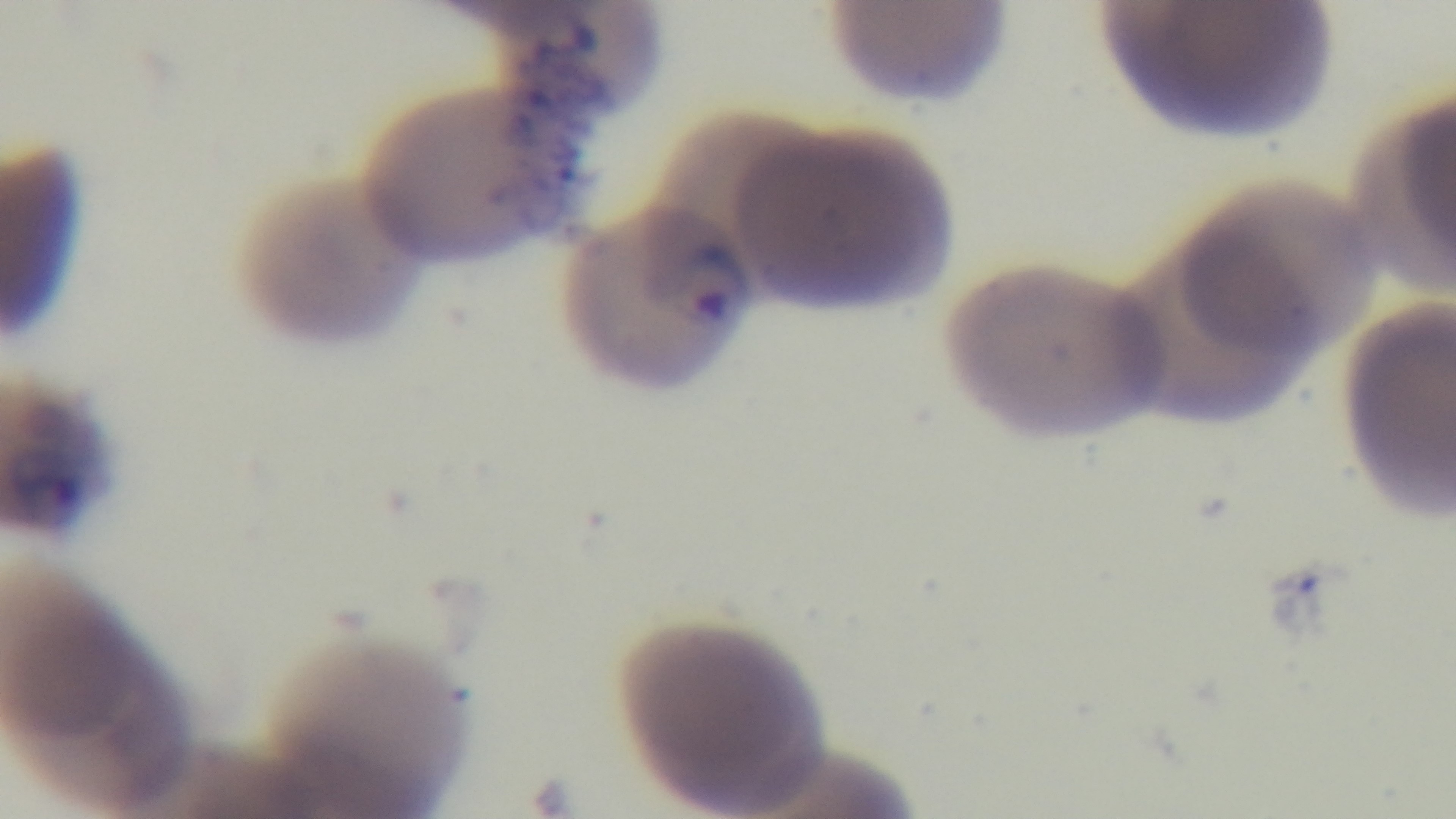 Oil-immersion objective, 100x. Malaria status: positive. One field from the slide. Giemsa-stained. Light microscopy. Mounted 4K digital camera. Preparation: thin smear.